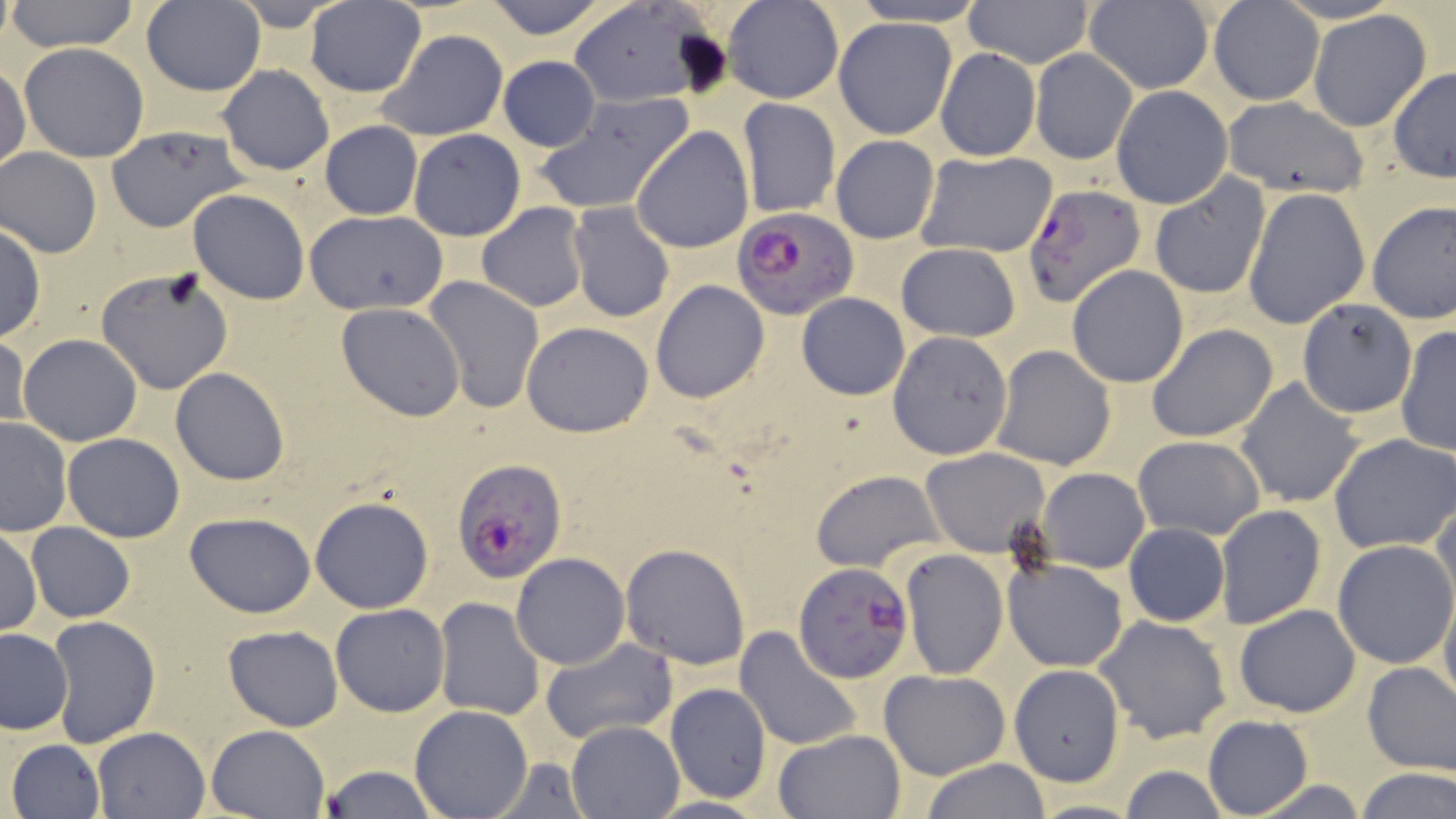 Approximate bounding boxes as (x1,y1)-(x2,y2) corner pairs in pixels. Plasmodium falciparum-infected red blood cell locations: (1021,185)-(1143,308), (732,205)-(859,320), (451,460)-(567,584), (792,565)-(918,684). Uninfected red blood cell locations: (6,0)-(141,52), (304,0)-(426,97), (480,0)-(615,40), (1208,0)-(1326,104), (140,1)-(265,96), (567,1)-(719,109), (723,1)-(844,103), (962,1)-(1095,68), (842,2)-(995,28), (1082,2)-(1214,92), (1307,10)-(1433,133), (833,17)-(958,139), (376,28)-(508,142), (18,43)-(149,164), (1029,48)-(1138,164), (936,49)-(1040,162), (498,56)-(601,152), (0,62)-(29,174), (217,64)-(334,175), (1388,66)-(1456,181), (1112,85)-(1232,208), (533,92)-(695,217), (1222,94)-(1368,200), (737,98)-(840,217), (320,120)-(423,220), (103,124)-(250,233), (630,125)-(754,254), (408,129)-(526,241), (831,135)-(940,244), (1,149)-(102,258), (914,149)-(1058,258), (1149,172)-(1271,299), (1242,187)-(1370,329), (187,189)-(311,306), (1366,201)-(1456,324), (476,202)-(588,313), (567,203)-(675,323), (302,209)-(449,313), (0,222)-(46,342), (895,243)-(1021,342), (1066,264)-(1190,388), (96,266)-(237,393), (423,275)-(543,412), (650,279)-(770,403), (796,292)-(910,400), (1296,299)-(1417,418), (336,302)-(464,422), (522,321)-(654,437), (1147,325)-(1277,442), (1395,325)-(1455,456), (886,330)-(1014,460), (1,333)-(30,436), (17,334)-(142,446), (989,344)-(1117,469), (170,368)-(289,484), (1236,377)-(1365,509), (0,416)-(73,536), (63,432)-(185,542), (1327,433)-(1456,554), (1133,434)-(1265,539), (921,447)-(1050,557), (1038,467)-(1150,574), (810,469)-(944,571), (1432,492)-(1456,617), (310,495)-(435,614), (1214,503)-(1327,630), (185,511)-(317,618), (25,523)-(135,622), (1123,523)-(1230,627), (1,525)-(42,637), (1332,541)-(1455,667), (619,543)-(751,669), (900,549)-(1008,679), (511,552)-(629,670), (1002,555)-(1128,672), (1439,585)-(1456,712), (433,599)-(544,720), (331,603)-(449,716), (1233,603)-(1361,717), (46,614)-(161,748), (1095,615)-(1231,743), (224,626)-(344,730), (736,626)-(863,752), (0,628)-(73,735), (540,637)-(677,745), (1361,661)-(1456,776), (1010,665)-(1125,785), (880,669)-(1010,779), (666,684)-(771,801), (409,704)-(532,818), (1203,716)-(1313,818), (566,720)-(687,818), (205,724)-(331,817), (93,726)-(210,818), (775,729)-(906,818), (6,738)-(104,819), (483,757)-(596,816), (921,759)-(1052,819), (318,764)-(438,819), (1118,765)-(1229,819), (1353,768)-(1455,819), (1238,777)-(1373,817), (1022,799)-(1149,818). Slide-level diagnosis: Plasmodium falciparum. Image is 1456×819 pixels. Optical microscopy. May-Grünwald-Giemsa-stained preparation. Thin blood film. Captured at 1000x magnification. One field of a larger specimen.